Name the parasite shown.
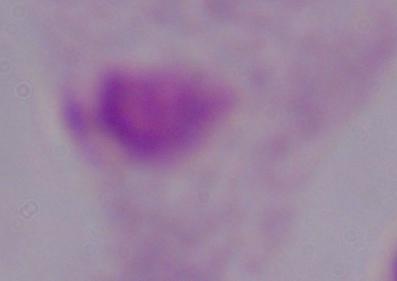
A trichomonad.

{
  "modality": "micrograph",
  "magnification": "1000x"
}